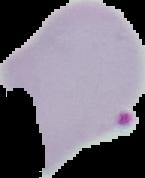 Image is 145×178 pixels. The area outside the segmented cell region is set to black. From a thin blood smear. Malaria status: parasitized.